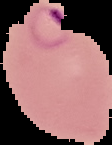

From a thin blood smear. Malaria status: parasitized. Segmented cell region on a black background. Image is 112×145 pixels.